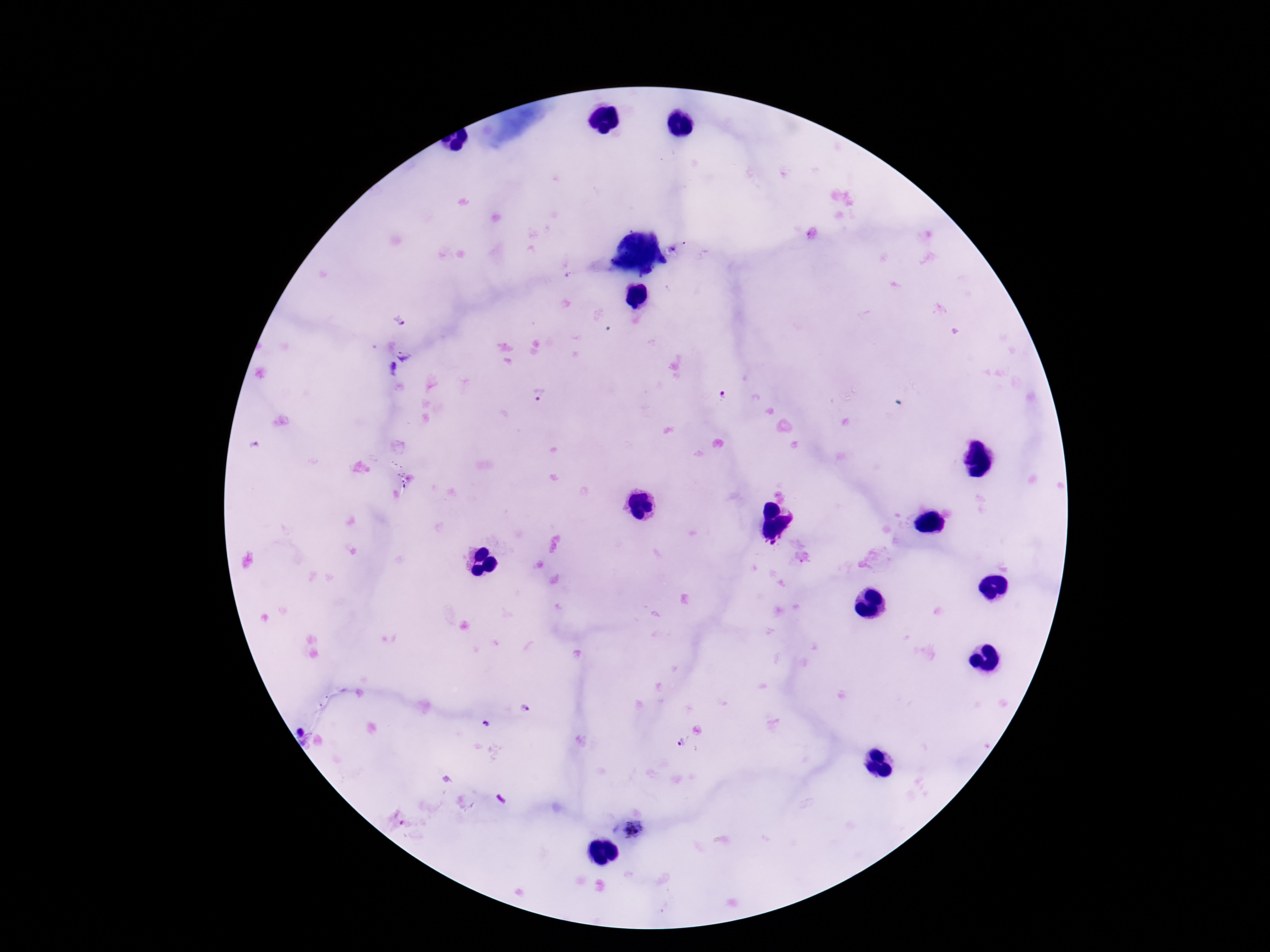
Approximate centers as (x, y) in pixels. Plasmodium parasite locations: (399, 321), (404, 354), (539, 396), (725, 397), (525, 709), (682, 742), (633, 830). Single field of view. Giemsa-stained preparation. 100x magnification. Patient malaria status: infected. Smartphone photograph taken through the microscope eyepiece. Thick blood smear. Image is 1270×952 pixels.